Identify the blood parasite species.
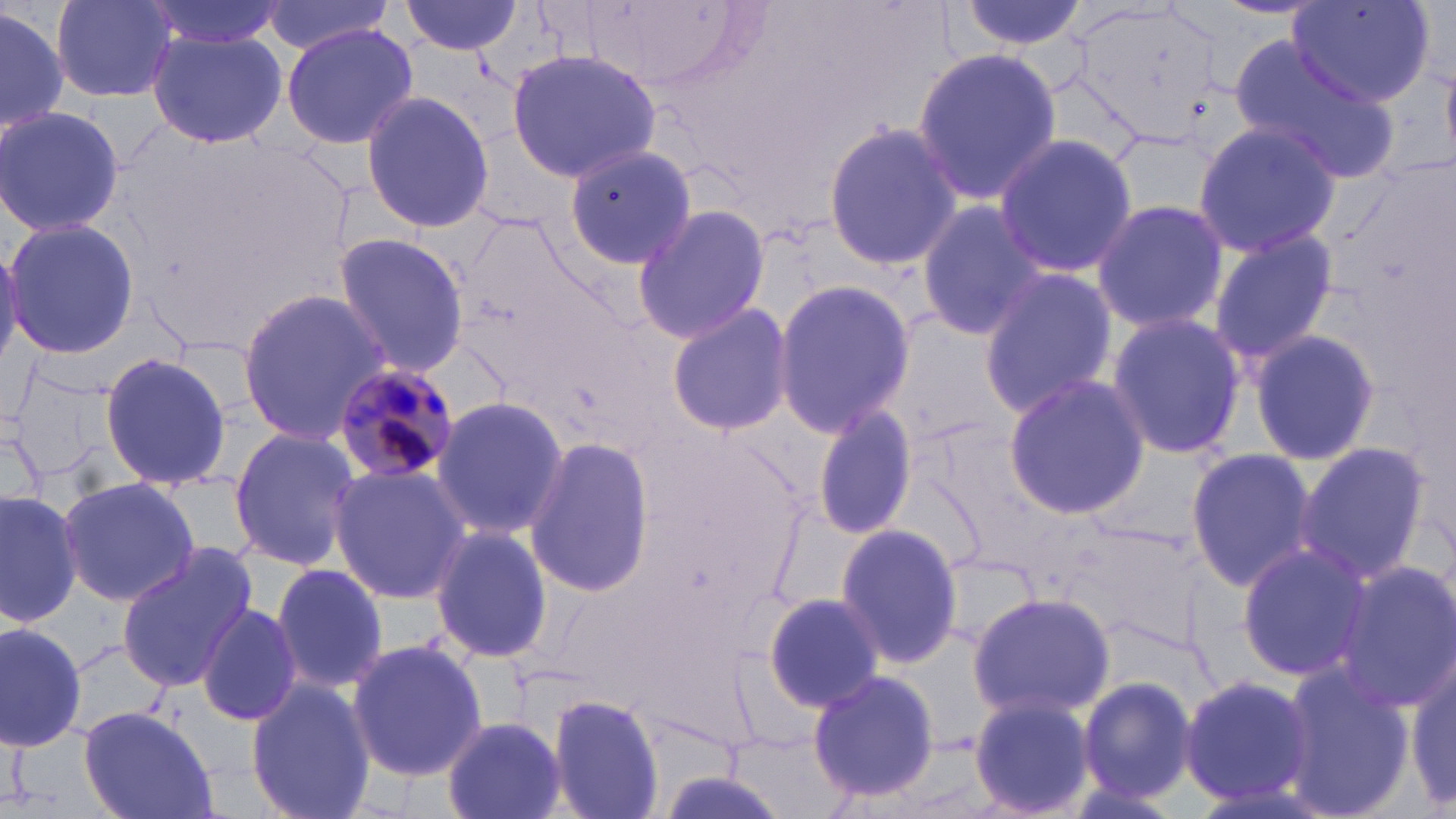
Plasmodium malariae.

field of view = single
Plasmodium malariae-infected red blood cell locations = approximate bounding boxes as (x1, y1, x2, y2) in pixels: (331, 360, 463, 489)
magnification = 1000x
uninfected red blood cell locations = approximate bounding boxes as (x1, y1, x2, y2) in pixels: (51, 0, 178, 102), (136, 0, 288, 55), (257, 0, 402, 55), (400, 0, 522, 55), (950, 0, 1092, 54), (1289, 1, 1431, 108), (0, 3, 70, 137), (281, 22, 418, 151), (146, 28, 288, 150), (1226, 38, 1399, 183), (911, 47, 1063, 207), (506, 49, 665, 180), (358, 88, 495, 238), (0, 104, 125, 240), (820, 120, 961, 273), (1191, 120, 1344, 258), (991, 132, 1138, 279), (565, 139, 703, 272), (1090, 197, 1230, 333), (913, 199, 1052, 340), (630, 202, 773, 346), (1, 216, 140, 359), (1203, 227, 1340, 373), (330, 232, 471, 376), (0, 239, 23, 374), (975, 267, 1122, 419), (770, 279, 915, 438), (236, 289, 396, 445), (665, 303, 797, 438), (1104, 311, 1247, 460), (1246, 329, 1381, 467), (98, 350, 231, 493), (1001, 373, 1148, 521), (431, 396, 569, 540), (810, 402, 918, 540), (227, 427, 362, 573), (523, 437, 657, 597), (1293, 442, 1433, 583), (1183, 444, 1320, 594), (329, 464, 471, 605), (58, 477, 199, 609), (0, 486, 81, 627), (833, 521, 964, 671), (1061, 521, 1203, 652), (429, 525, 552, 665), (1234, 541, 1371, 683), (114, 545, 258, 691), (933, 549, 1042, 654), (760, 552, 957, 701), (1333, 558, 1455, 714), (270, 563, 392, 694), (762, 591, 886, 714), (966, 591, 1116, 720), (196, 602, 303, 729), (0, 620, 90, 753), (346, 639, 486, 781), (1408, 655, 1455, 812), (1276, 659, 1417, 819), (807, 669, 944, 805), (1177, 673, 1317, 809), (246, 678, 376, 819), (1079, 678, 1198, 802), (548, 694, 665, 819), (966, 694, 1097, 819), (77, 706, 218, 819), (442, 715, 565, 819)
image size = 1456×819 pixels
preparation = thin blood smear
modality = optical microscopy
stain = May-Grünwald-Giemsa